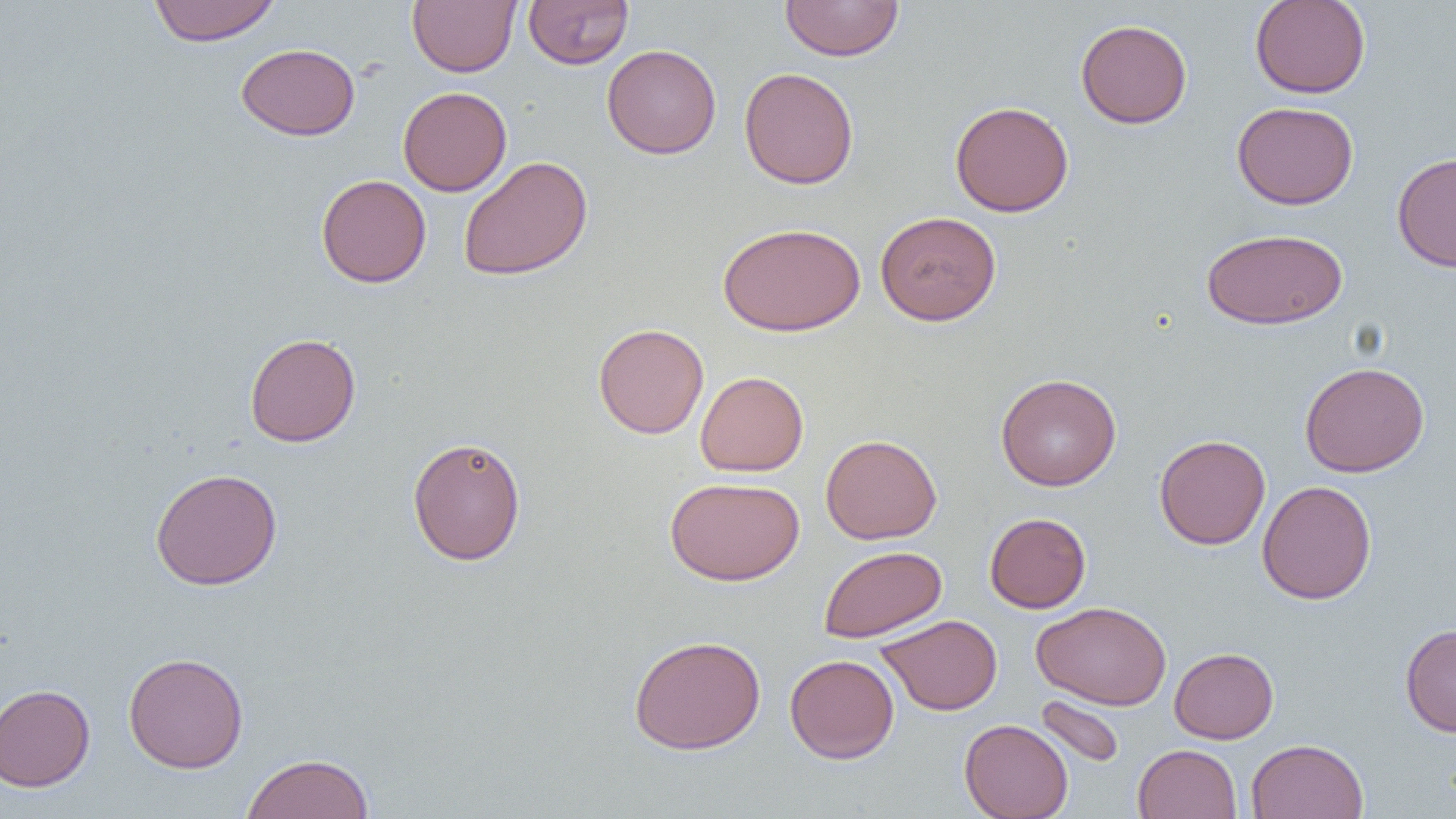

Summary:
  - Coordinate format: approximate bounding boxes as named x1/y1/x2/y2 corners in pixels
  - Uninfected red blood cell locations: (x1=148, y1=0, x2=281, y2=46), (x1=407, y1=0, x2=520, y2=77), (x1=523, y1=0, x2=634, y2=69), (x1=779, y1=0, x2=904, y2=61), (x1=1250, y1=0, x2=1371, y2=98), (x1=1075, y1=19, x2=1192, y2=128), (x1=235, y1=43, x2=360, y2=140), (x1=601, y1=44, x2=721, y2=159), (x1=739, y1=67, x2=859, y2=189), (x1=397, y1=86, x2=512, y2=196), (x1=950, y1=100, x2=1074, y2=217), (x1=1232, y1=101, x2=1359, y2=209), (x1=1392, y1=151, x2=1456, y2=272), (x1=457, y1=155, x2=593, y2=281), (x1=316, y1=174, x2=431, y2=288), (x1=875, y1=211, x2=1001, y2=326), (x1=717, y1=222, x2=865, y2=337), (x1=1201, y1=228, x2=1348, y2=329), (x1=593, y1=322, x2=709, y2=439), (x1=245, y1=333, x2=361, y2=447), (x1=1300, y1=361, x2=1430, y2=477), (x1=695, y1=371, x2=809, y2=476), (x1=995, y1=373, x2=1121, y2=491), (x1=1154, y1=433, x2=1271, y2=550), (x1=820, y1=434, x2=942, y2=544), (x1=407, y1=436, x2=526, y2=565), (x1=150, y1=468, x2=283, y2=591), (x1=665, y1=476, x2=804, y2=586), (x1=1257, y1=480, x2=1377, y2=604), (x1=984, y1=512, x2=1091, y2=613), (x1=818, y1=545, x2=947, y2=643), (x1=1032, y1=600, x2=1171, y2=710), (x1=876, y1=614, x2=1002, y2=716), (x1=1400, y1=623, x2=1456, y2=737), (x1=629, y1=634, x2=766, y2=755), (x1=1169, y1=647, x2=1279, y2=743), (x1=123, y1=651, x2=249, y2=773), (x1=784, y1=654, x2=899, y2=763), (x1=0, y1=683, x2=95, y2=791), (x1=1034, y1=695, x2=1126, y2=768), (x1=959, y1=719, x2=1073, y2=819), (x1=1246, y1=738, x2=1368, y2=819), (x1=1133, y1=743, x2=1241, y2=819), (x1=241, y1=752, x2=374, y2=819)
  - Slide-level diagnosis: negative for blood parasites
  - Modality: light microscopy
  - Magnification: 1000x
  - Field of view: one of a larger specimen
  - Image size: 1456×819 pixels
  - Preparation: thin blood film